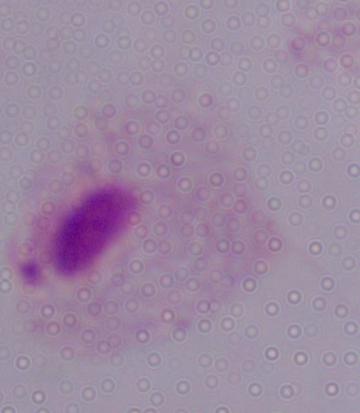

identification = trichomonad
modality = photomicrograph
magnification = 1000x